Locate every Plasmodium falciparum parasite and identify its life-cycle stage.
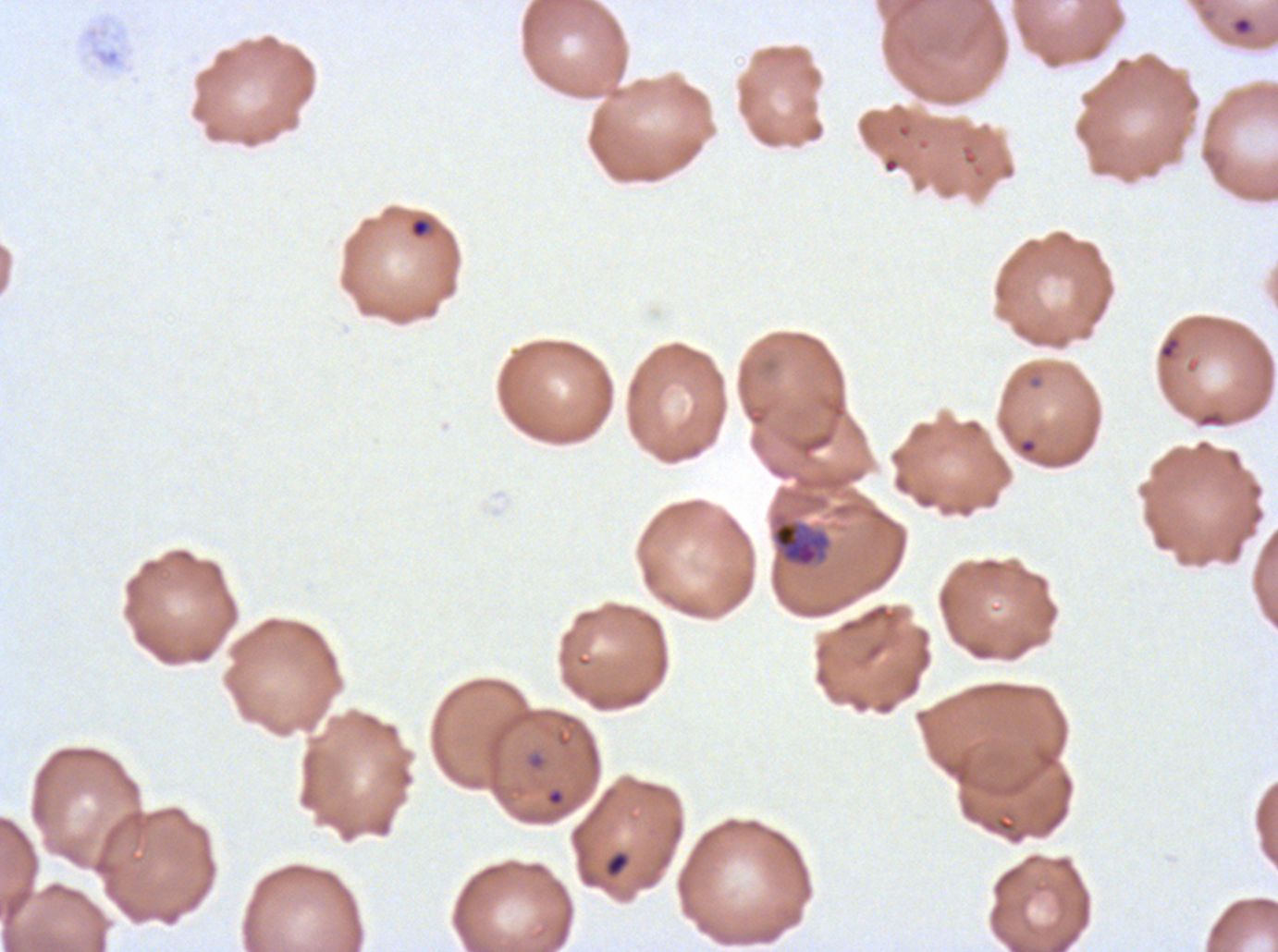

Approximate bounding boxes as [x1, y1, x2, y2] in pixels.
Rings: [1232, 16, 1252, 35], [410, 217, 430, 238], [1159, 336, 1181, 360], [546, 788, 564, 806].
Mid trophozoites: [771, 519, 831, 568].
No late-ring/early-trophozoite forms, late trophozoites, early schizonts, late schizonts, segmenters, or gametocytes observed.

debris locations = [605, 851, 630, 877]
field of view = sub-image separated from a larger composite
life-cycle stages observed = ring, mid trophozoite
image size = 1278×952 pixels
preparation = thin blood smear
stain = Giemsa
specimen = Plasmodium falciparum cultured ex vivo for 24 to 48 hours, from a patient in The Gambia